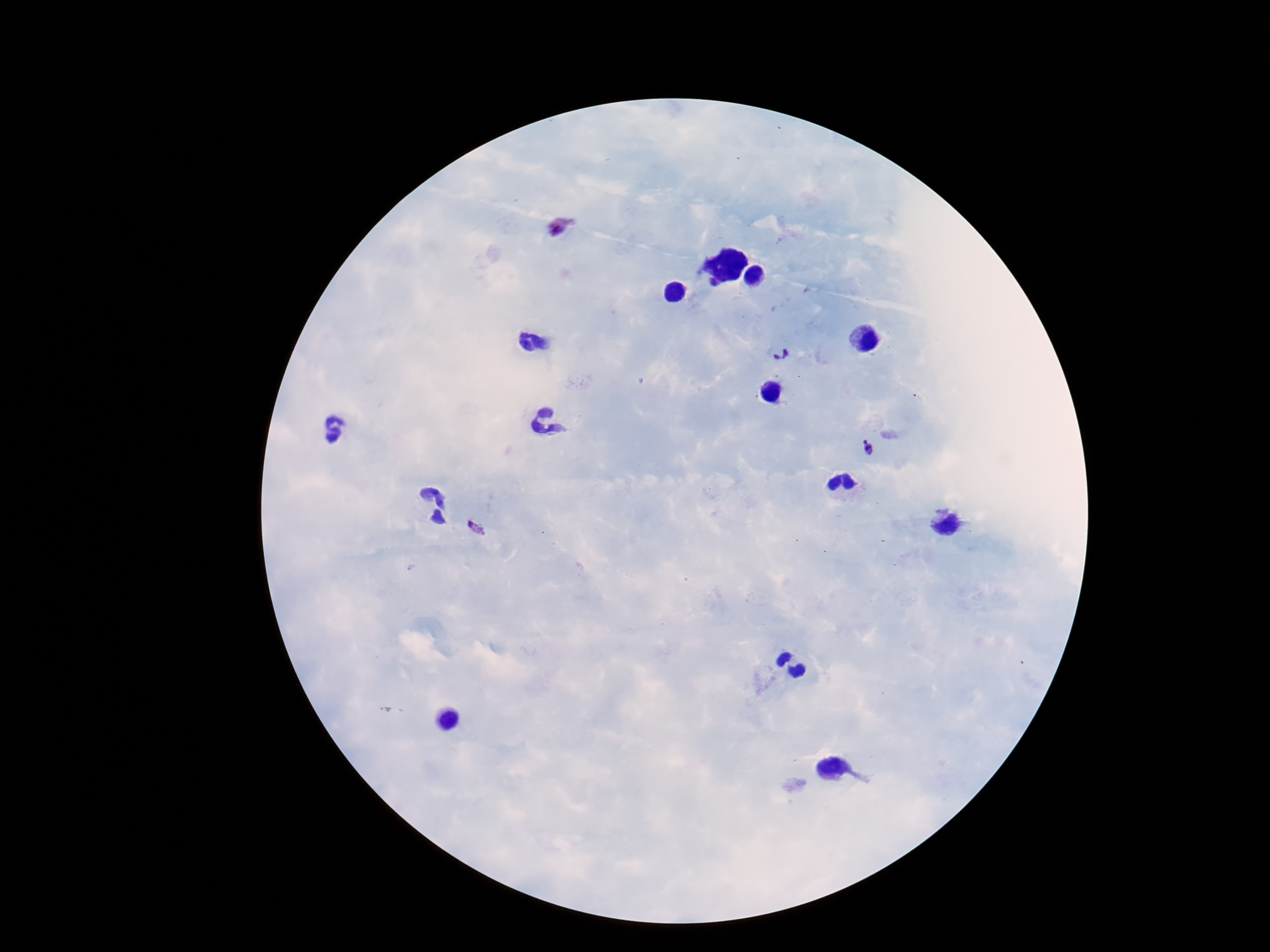

stain = Giemsa
image size = 1270×952 pixels
preparation = thick peripheral-blood smear
patient malaria status = infected
magnification = 100x
capture = smartphone camera through the microscope eyepiece
field of view = one from this slide
Plasmodium parasite locations = approximate centers as (x, y) in pixels: (560, 224), (781, 354), (866, 449), (475, 529)